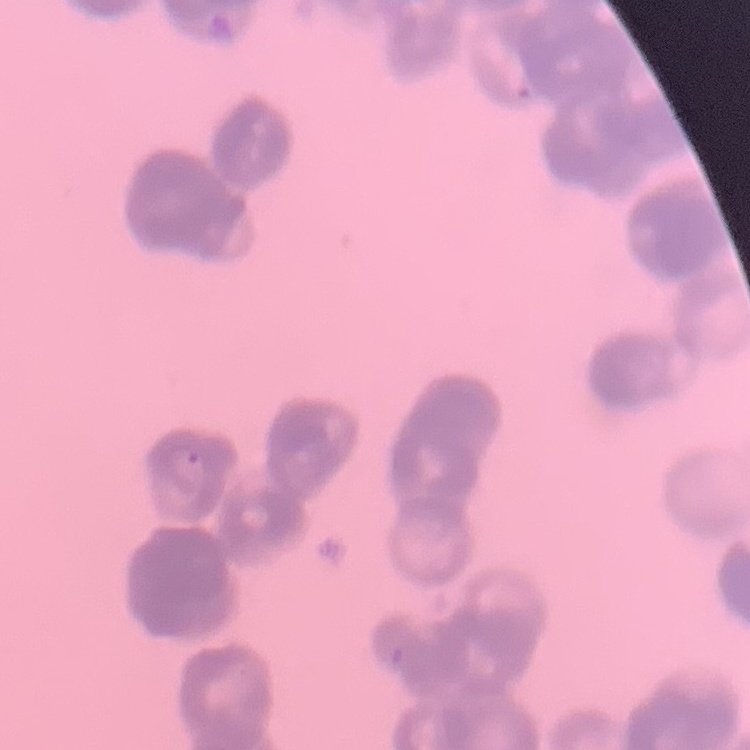

erythrocyte_morphology: rouleaux formation
image_type: square crop of a larger photomicrograph
stain: Field's or Giemsa
preparation: thin blood smear